Classify this cell by malaria status.
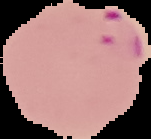

Parasitized.

preparation = thin blood film
image type = segmented cell region on a black background
image size = 151×139 pixels